Name the parasite shown.
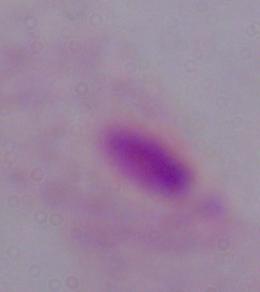

This is a trichomonad.

Summary:
  - Magnification: 1000x
  - Modality: photomicrograph